Locate every blood parasite and identify its species.
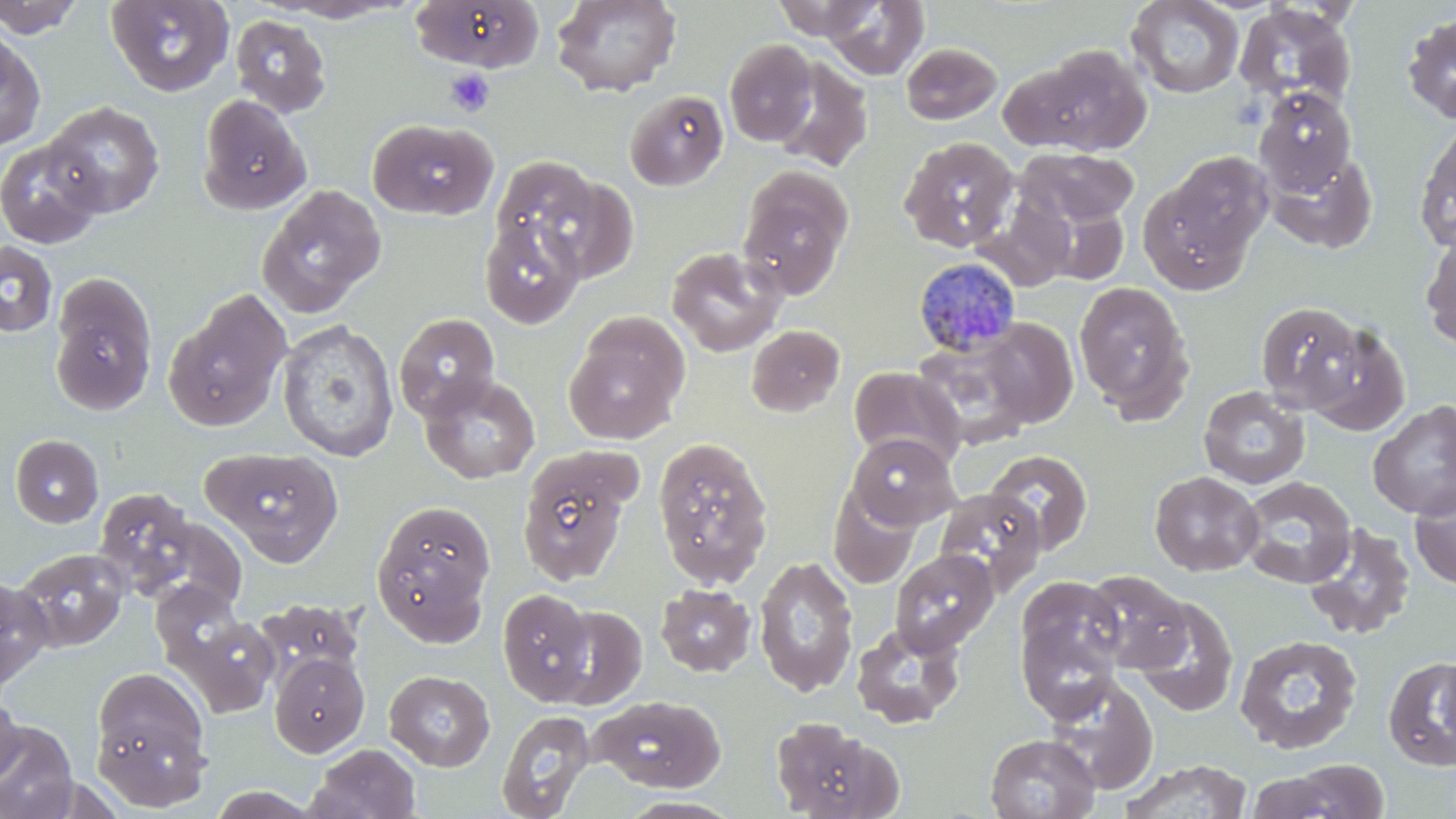

Approximate bounding boxes as [x1, y1, x2, y2] in pixels.
Plasmodium malariae-infected red blood cells: [913, 256, 1023, 357].
No Plasmodium falciparum, Plasmodium ovale, Plasmodium vivax, Babesia divergens, or Trypanosoma brucei observed.

Summary:
  - Platelet locations: [445, 68, 494, 116]
  - Uninfected red blood cell locations: [0, 0, 87, 38], [105, 0, 234, 97], [551, 0, 682, 97], [771, 0, 882, 41], [1125, 0, 1246, 99], [272, 1, 413, 23], [410, 1, 545, 72], [821, 1, 929, 80], [1233, 3, 1357, 112], [1401, 12, 1456, 124], [230, 15, 332, 117], [0, 25, 45, 152], [724, 39, 817, 147], [901, 42, 1003, 125], [1006, 44, 1152, 156], [770, 57, 873, 172], [1252, 86, 1358, 196], [625, 89, 728, 191], [198, 94, 311, 216], [41, 101, 165, 219], [367, 117, 497, 220], [1414, 121, 1456, 252], [899, 136, 1019, 252], [1, 138, 105, 249], [1016, 148, 1139, 227], [1264, 148, 1377, 252], [1151, 152, 1273, 276], [490, 156, 601, 262], [737, 166, 853, 299], [522, 171, 638, 284], [256, 184, 387, 318], [976, 197, 1079, 291], [1033, 198, 1131, 287], [479, 215, 586, 329], [1420, 229, 1456, 351], [0, 241, 58, 338], [665, 246, 788, 357], [49, 273, 158, 416], [1073, 281, 1194, 419], [164, 288, 292, 431], [1255, 301, 1368, 415], [394, 313, 500, 422], [563, 317, 687, 445], [978, 318, 1079, 428], [276, 320, 399, 462], [1300, 321, 1410, 436], [745, 324, 845, 417], [911, 337, 1037, 450], [848, 366, 965, 469], [418, 373, 541, 484], [1197, 386, 1309, 489], [1367, 400, 1456, 520], [846, 432, 960, 530], [10, 434, 103, 528], [653, 436, 774, 588], [203, 447, 343, 566], [517, 447, 639, 586], [983, 449, 1093, 555], [1149, 470, 1264, 576], [1237, 476, 1356, 588], [1409, 483, 1456, 591], [828, 484, 922, 590], [93, 487, 201, 596], [932, 487, 1047, 592], [371, 499, 497, 643], [1303, 523, 1416, 640], [13, 548, 129, 653], [889, 549, 998, 657], [753, 555, 859, 697], [1083, 571, 1192, 673], [1013, 575, 1130, 719], [0, 576, 53, 691], [656, 583, 756, 677], [498, 589, 595, 704], [1131, 596, 1239, 718], [257, 598, 363, 689], [548, 604, 647, 710], [180, 614, 280, 717], [851, 622, 966, 729], [1234, 634, 1363, 755], [269, 652, 369, 757], [1435, 653, 1456, 761], [1383, 656, 1456, 772], [89, 665, 212, 806], [384, 670, 495, 771], [1041, 676, 1158, 796], [0, 690, 23, 786], [593, 695, 727, 793], [496, 709, 595, 819], [770, 717, 901, 818], [0, 721, 79, 819], [985, 733, 1101, 818], [307, 743, 422, 819], [1120, 759, 1254, 818], [1266, 761, 1392, 818], [618, 796, 743, 818]
  - Slide-level diagnosis: Plasmodium malariae
  - Image size: 1456×819 pixels
  - Field of view: one of a larger specimen
  - Modality: light microscopy
  - Preparation: thin blood film
  - Magnification: 1000x
  - Stain: May-Grünwald-Giemsa